Assess this cell for malaria.
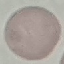
It is uninfected.

capture = smartphone camera at the microscope eyepiece
image type = automatically extracted cell patch, resized to 64 × 64 pixels
stain = Giemsa
preparation = thin blood smear